Name the blood parasite species.
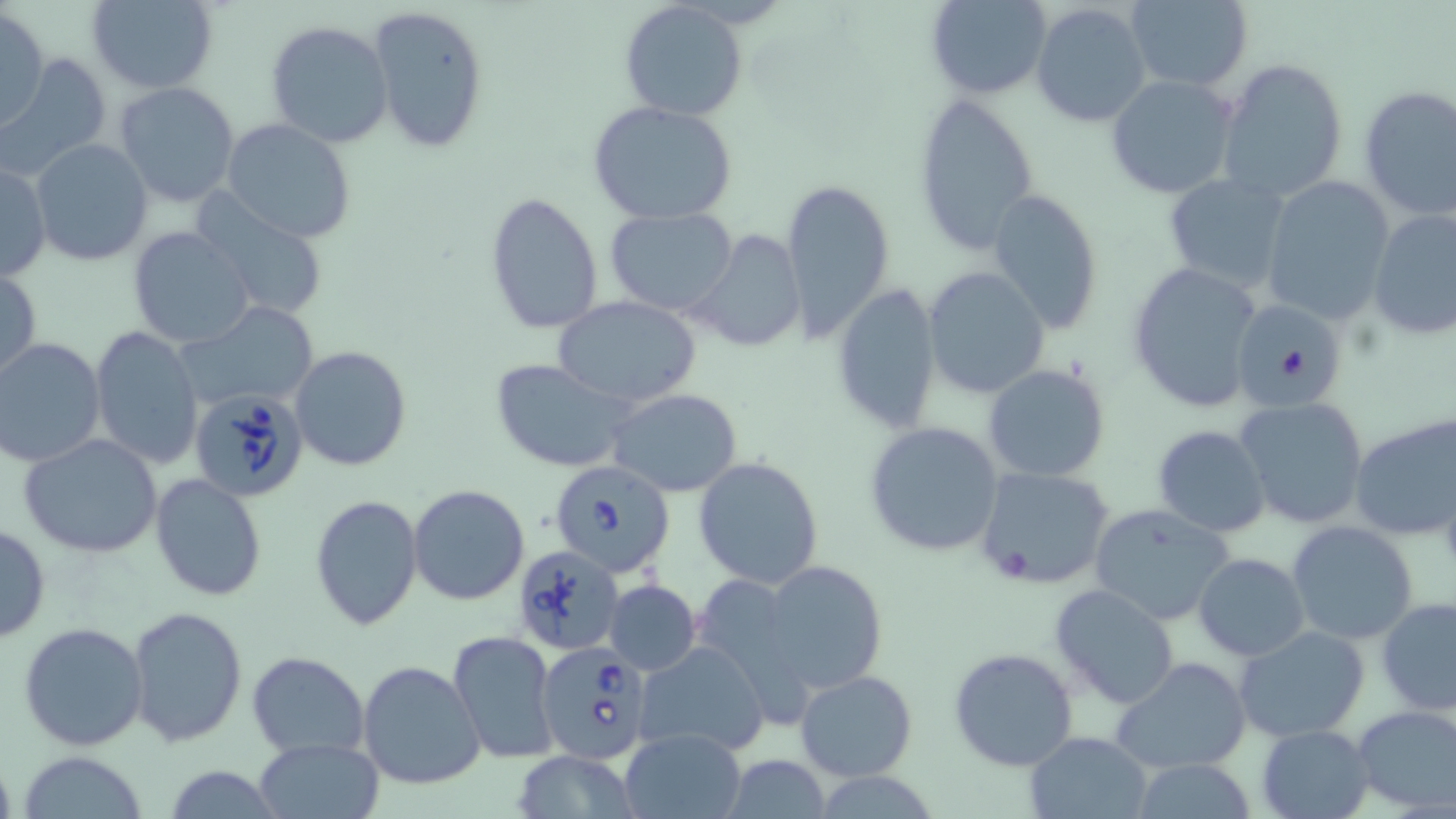

Babesia divergens.

Summary:
  - Coordinate format: approximate bounding boxes as (x1, y1, x2, y2) in pixels
  - Babesia divergens-infected red blood cell locations: (186, 386, 313, 503), (548, 457, 676, 578), (514, 545, 623, 654), (538, 641, 657, 764)
  - Uninfected red blood cell locations: (85, 0, 219, 93), (926, 0, 1054, 99), (1122, 0, 1253, 92), (619, 1, 749, 120), (1030, 3, 1152, 128), (366, 5, 490, 155), (1, 7, 49, 133), (264, 18, 395, 150), (4, 54, 112, 177), (1216, 58, 1349, 203), (1105, 73, 1239, 198), (113, 82, 241, 209), (1357, 85, 1456, 220), (911, 93, 1041, 257), (588, 101, 738, 225), (222, 120, 356, 244), (30, 138, 156, 267), (0, 160, 50, 283), (1161, 173, 1291, 295), (1262, 175, 1394, 323), (781, 176, 895, 339), (986, 188, 1104, 337), (484, 192, 604, 336), (193, 194, 332, 321), (603, 208, 741, 315), (1367, 209, 1456, 340), (127, 226, 257, 349), (689, 229, 809, 352), (1127, 260, 1265, 415), (1, 267, 42, 382), (924, 267, 1050, 400), (831, 284, 943, 432), (552, 294, 701, 410), (1232, 298, 1347, 411), (179, 303, 319, 413), (90, 326, 204, 472), (1, 338, 106, 468), (289, 345, 411, 472), (492, 359, 634, 472), (983, 363, 1111, 482), (608, 388, 744, 496), (1234, 396, 1370, 529), (1348, 411, 1456, 540), (863, 420, 1005, 558), (1151, 424, 1272, 535), (19, 434, 165, 559), (693, 456, 825, 590), (975, 466, 1114, 589), (150, 473, 268, 603), (408, 484, 528, 605), (311, 493, 423, 632), (1088, 504, 1236, 627), (1286, 519, 1419, 645), (0, 522, 50, 643), (1193, 553, 1310, 660), (760, 559, 888, 697), (604, 579, 700, 675), (1048, 583, 1179, 708), (1375, 597, 1456, 716), (125, 604, 249, 747), (20, 623, 149, 751), (1233, 626, 1372, 744), (448, 630, 559, 762), (636, 642, 771, 758), (950, 647, 1078, 772), (246, 651, 369, 756), (1111, 655, 1252, 775), (358, 660, 486, 790), (797, 671, 918, 781), (1351, 704, 1456, 813), (1256, 723, 1376, 818), (617, 729, 747, 818), (1023, 731, 1153, 819), (253, 737, 383, 818), (509, 750, 642, 818), (17, 752, 151, 818), (720, 757, 834, 818), (1127, 759, 1263, 816), (162, 766, 284, 818)
  - Magnification: 1000x
  - Image size: 1456×819 pixels
  - Preparation: thin blood film
  - Modality: light microscopy
  - Stain: May-Grünwald-Giemsa
  - Field of view: one of a larger specimen